Name the cell type shown.
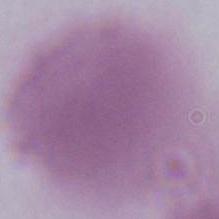

An erythrocyte.

Summary:
  - Magnification: 1000x
  - Modality: photomicrograph